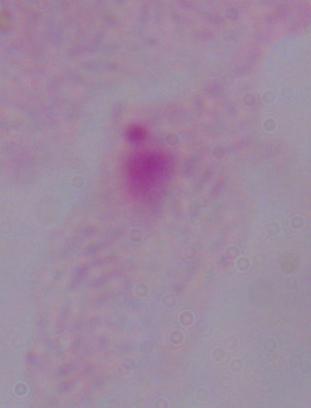

A trichomonad is shown. Captured at 1000x magnification. Micrograph.